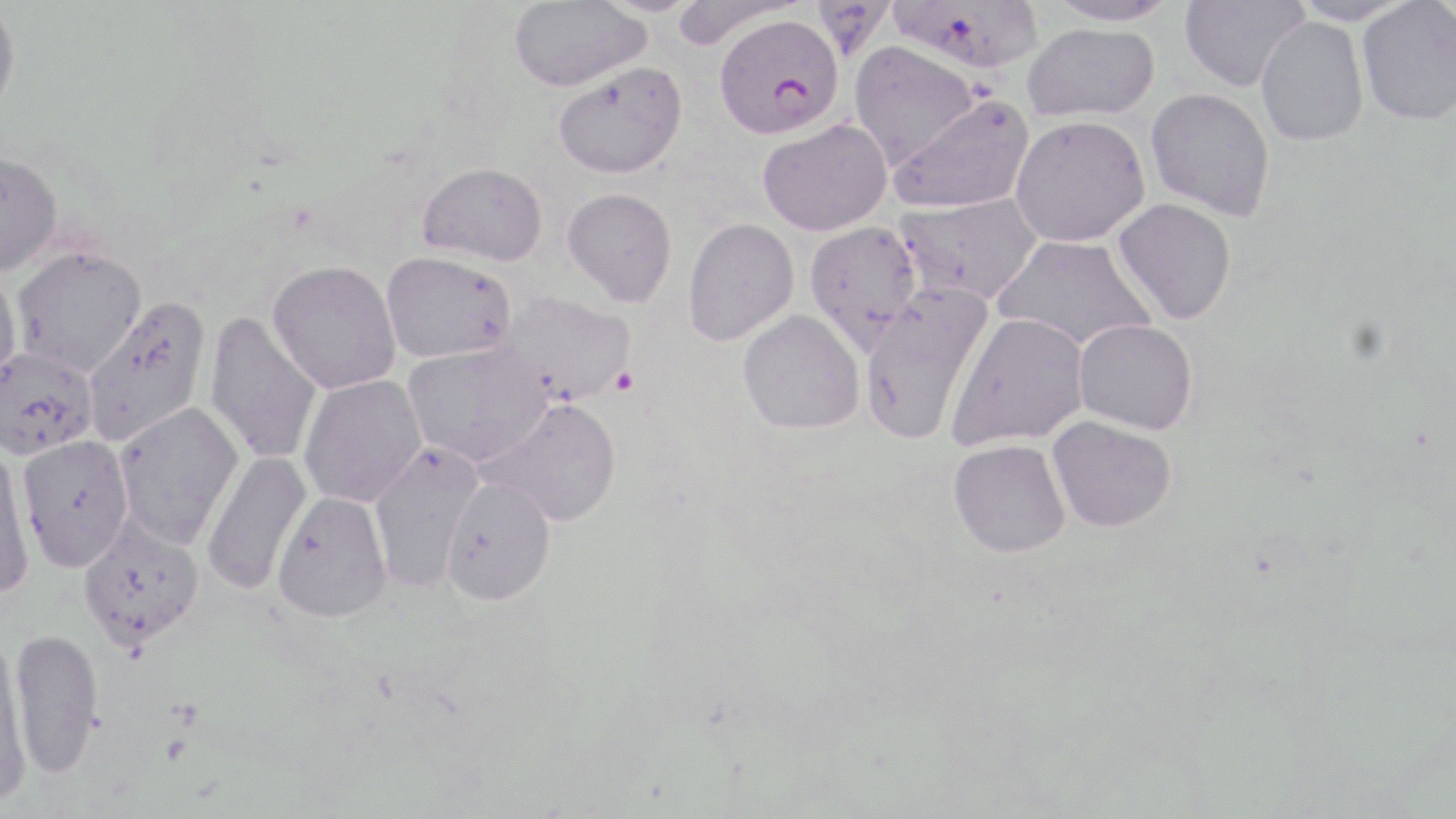
Summary:
  - Coordinate format: approximate bounding boxes as (x1,y1)-(x2,y2) corner pairs in pixels
  - Plasmodium falciparum-infected red blood cell locations: (713,12)-(843,139)
  - Uninfected red blood cell locations: (887,0)-(1043,73), (1044,0)-(1178,27), (1179,0)-(1309,92), (1289,0)-(1413,26), (508,1)-(650,91), (1356,1)-(1456,125), (0,2)-(21,120), (1256,16)-(1369,146), (1023,23)-(1159,122), (848,41)-(980,169), (553,62)-(687,180), (1146,87)-(1275,221), (887,93)-(1035,214), (1010,115)-(1150,247), (758,118)-(892,236), (0,149)-(62,275), (417,162)-(548,267), (562,187)-(677,307), (894,193)-(1043,307), (1113,198)-(1237,324), (682,218)-(799,346), (804,220)-(922,352), (992,235)-(1157,353), (10,245)-(146,378), (380,250)-(516,363), (267,260)-(401,394), (0,267)-(22,394), (859,283)-(994,445), (498,290)-(636,406), (82,296)-(212,447), (737,310)-(865,434), (203,311)-(323,465), (947,312)-(1089,450), (1073,319)-(1198,434), (403,340)-(552,467), (0,347)-(98,459), (298,374)-(427,507), (483,397)-(623,526), (113,401)-(244,549), (1048,415)-(1176,532), (17,434)-(134,572), (949,439)-(1071,557), (368,441)-(484,591), (0,444)-(36,601), (201,451)-(312,595), (441,477)-(556,605), (273,490)-(391,622), (77,517)-(205,651), (9,626)-(103,778), (0,636)-(32,799)
  - Slide-level diagnosis: Plasmodium falciparum
  - Stain: May-Grünwald-Giemsa
  - Image size: 1456×819 pixels
  - Field of view: one of a larger specimen
  - Preparation: thin blood film
  - Modality: optical microscopy
  - Magnification: 1000x